Locate and identify every blood parasite.
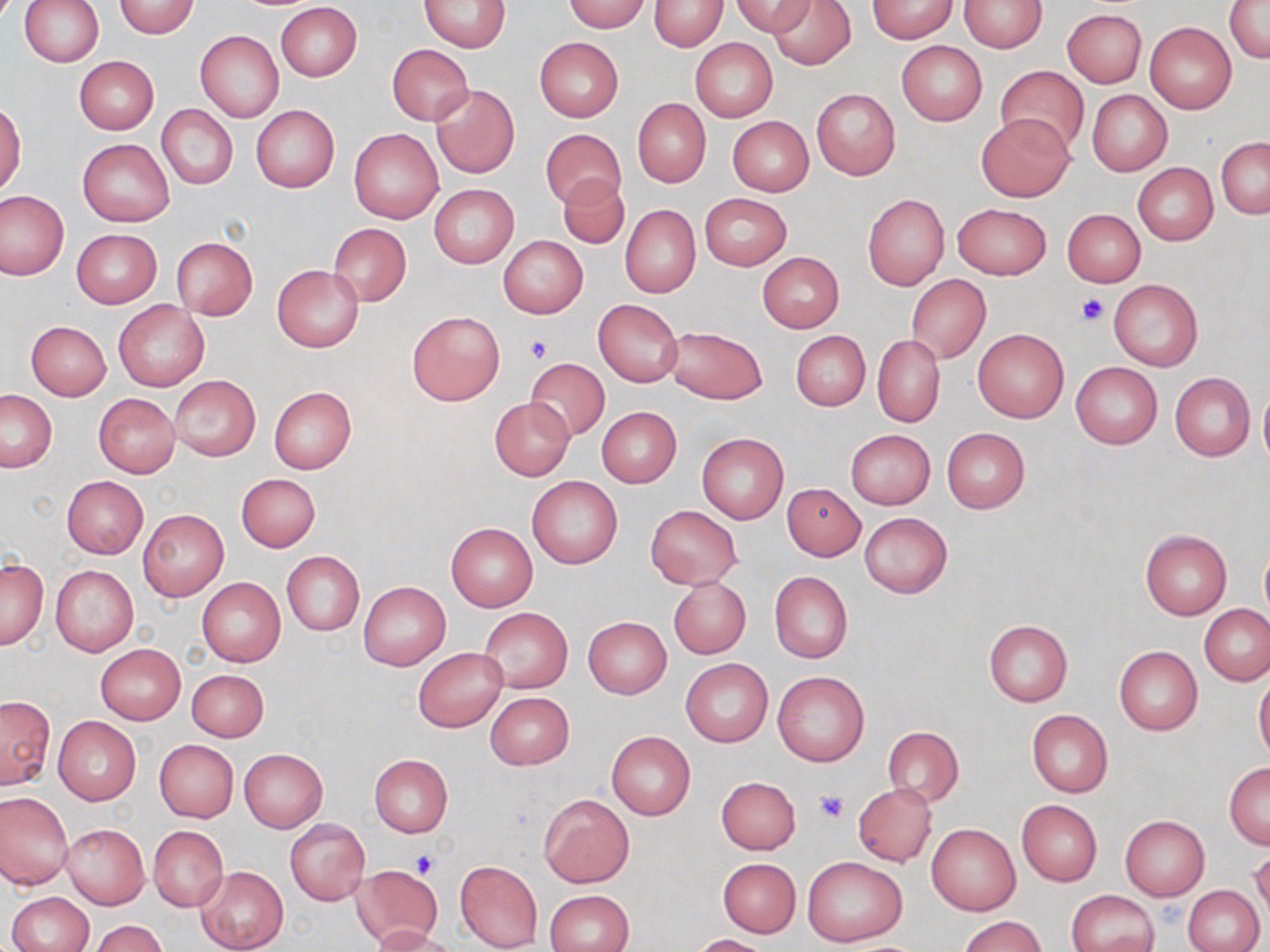

No blood parasites observed.

Approximate bounding boxes as named x1/y1/x2/y2 corners in pixels. Platelet locations: (x1=1074, y1=294, x2=1109, y2=326), (x1=525, y1=333, x2=553, y2=364), (x1=815, y1=789, x2=847, y2=823), (x1=411, y1=849, x2=441, y2=878). Uninfected red blood cell locations: (x1=19, y1=0, x2=103, y2=67), (x1=561, y1=0, x2=650, y2=32), (x1=733, y1=0, x2=814, y2=37), (x1=766, y1=0, x2=856, y2=70), (x1=867, y1=0, x2=957, y2=41), (x1=960, y1=0, x2=1047, y2=52), (x1=419, y1=1, x2=509, y2=51), (x1=649, y1=1, x2=728, y2=50), (x1=1225, y1=1, x2=1270, y2=66), (x1=113, y1=2, x2=199, y2=38), (x1=276, y1=3, x2=362, y2=81), (x1=1062, y1=9, x2=1146, y2=88), (x1=1145, y1=21, x2=1236, y2=113), (x1=196, y1=30, x2=284, y2=122), (x1=534, y1=37, x2=623, y2=123), (x1=690, y1=38, x2=777, y2=122), (x1=895, y1=41, x2=985, y2=126), (x1=387, y1=44, x2=473, y2=125), (x1=74, y1=56, x2=159, y2=134), (x1=996, y1=66, x2=1089, y2=155), (x1=430, y1=84, x2=519, y2=179), (x1=811, y1=88, x2=900, y2=180), (x1=1088, y1=89, x2=1172, y2=176), (x1=633, y1=99, x2=711, y2=187), (x1=1, y1=101, x2=26, y2=195), (x1=157, y1=104, x2=238, y2=190), (x1=250, y1=105, x2=339, y2=192), (x1=975, y1=113, x2=1072, y2=201), (x1=727, y1=116, x2=813, y2=196), (x1=540, y1=127, x2=626, y2=210), (x1=350, y1=128, x2=443, y2=223), (x1=1217, y1=137, x2=1269, y2=219), (x1=77, y1=139, x2=174, y2=226), (x1=1133, y1=164, x2=1218, y2=245), (x1=558, y1=175, x2=629, y2=249), (x1=430, y1=185, x2=518, y2=267), (x1=0, y1=191, x2=67, y2=280), (x1=699, y1=193, x2=792, y2=270), (x1=862, y1=194, x2=948, y2=290), (x1=952, y1=203, x2=1051, y2=280), (x1=620, y1=204, x2=700, y2=298), (x1=1062, y1=208, x2=1146, y2=287), (x1=329, y1=223, x2=412, y2=305), (x1=71, y1=229, x2=162, y2=308), (x1=498, y1=235, x2=587, y2=318), (x1=170, y1=236, x2=258, y2=320), (x1=757, y1=251, x2=844, y2=332), (x1=272, y1=265, x2=364, y2=352), (x1=906, y1=275, x2=991, y2=364), (x1=1109, y1=279, x2=1202, y2=371), (x1=593, y1=299, x2=683, y2=387), (x1=114, y1=300, x2=209, y2=390), (x1=407, y1=310, x2=504, y2=404), (x1=25, y1=320, x2=111, y2=400), (x1=663, y1=325, x2=768, y2=405), (x1=973, y1=329, x2=1069, y2=423), (x1=790, y1=331, x2=870, y2=411), (x1=872, y1=335, x2=945, y2=426), (x1=526, y1=359, x2=610, y2=440), (x1=1070, y1=362, x2=1162, y2=449), (x1=1171, y1=372, x2=1255, y2=461), (x1=170, y1=376, x2=261, y2=460), (x1=1258, y1=383, x2=1270, y2=471), (x1=269, y1=387, x2=356, y2=473), (x1=1, y1=390, x2=57, y2=472), (x1=93, y1=392, x2=180, y2=477), (x1=489, y1=398, x2=575, y2=479), (x1=596, y1=407, x2=681, y2=488), (x1=941, y1=428, x2=1030, y2=513), (x1=845, y1=429, x2=936, y2=510), (x1=696, y1=433, x2=788, y2=523), (x1=236, y1=473, x2=321, y2=551), (x1=61, y1=476, x2=149, y2=558), (x1=527, y1=476, x2=622, y2=568), (x1=782, y1=484, x2=865, y2=560), (x1=646, y1=506, x2=742, y2=589), (x1=138, y1=510, x2=228, y2=599), (x1=860, y1=512, x2=952, y2=598), (x1=446, y1=523, x2=538, y2=611), (x1=1140, y1=529, x2=1231, y2=619), (x1=1259, y1=546, x2=1270, y2=622), (x1=282, y1=551, x2=364, y2=635), (x1=0, y1=556, x2=48, y2=651), (x1=51, y1=565, x2=138, y2=657), (x1=769, y1=572, x2=853, y2=663), (x1=196, y1=577, x2=285, y2=667), (x1=669, y1=577, x2=751, y2=659), (x1=357, y1=581, x2=451, y2=670), (x1=1199, y1=604, x2=1270, y2=686), (x1=480, y1=607, x2=572, y2=693), (x1=583, y1=616, x2=671, y2=697), (x1=984, y1=620, x2=1072, y2=706), (x1=95, y1=644, x2=186, y2=724), (x1=1114, y1=646, x2=1203, y2=735), (x1=414, y1=647, x2=507, y2=733), (x1=682, y1=660, x2=772, y2=746), (x1=187, y1=668, x2=268, y2=741), (x1=772, y1=671, x2=870, y2=766), (x1=1254, y1=672, x2=1270, y2=762), (x1=485, y1=691, x2=574, y2=769), (x1=0, y1=695, x2=55, y2=789), (x1=1026, y1=709, x2=1113, y2=797), (x1=53, y1=716, x2=141, y2=803), (x1=883, y1=726, x2=963, y2=807), (x1=606, y1=731, x2=696, y2=819), (x1=154, y1=739, x2=238, y2=822), (x1=238, y1=749, x2=327, y2=832), (x1=369, y1=754, x2=452, y2=838), (x1=1225, y1=763, x2=1270, y2=848), (x1=717, y1=776, x2=800, y2=854), (x1=853, y1=782, x2=936, y2=866), (x1=0, y1=791, x2=74, y2=889), (x1=539, y1=794, x2=634, y2=888), (x1=1016, y1=800, x2=1102, y2=886), (x1=1118, y1=815, x2=1208, y2=902), (x1=286, y1=820, x2=370, y2=905), (x1=927, y1=822, x2=1020, y2=915), (x1=61, y1=824, x2=150, y2=908), (x1=148, y1=826, x2=228, y2=911), (x1=1249, y1=848, x2=1269, y2=922), (x1=802, y1=855, x2=907, y2=947), (x1=717, y1=858, x2=801, y2=938), (x1=454, y1=860, x2=543, y2=952), (x1=196, y1=865, x2=288, y2=952), (x1=351, y1=865, x2=442, y2=945), (x1=1184, y1=884, x2=1265, y2=952), (x1=546, y1=889, x2=634, y2=952), (x1=1066, y1=890, x2=1158, y2=952), (x1=6, y1=892, x2=93, y2=952), (x1=959, y1=916, x2=1046, y2=952), (x1=88, y1=919, x2=169, y2=952), (x1=366, y1=925, x2=455, y2=952), (x1=692, y1=934, x2=769, y2=952). Slide-level diagnosis: no evidence of blood parasites. Image is 1270×952 pixels. Optical microscopy. Thin blood film. Captured at 1000x magnification. Single field of view. May-Grünwald-Giemsa-stained preparation.